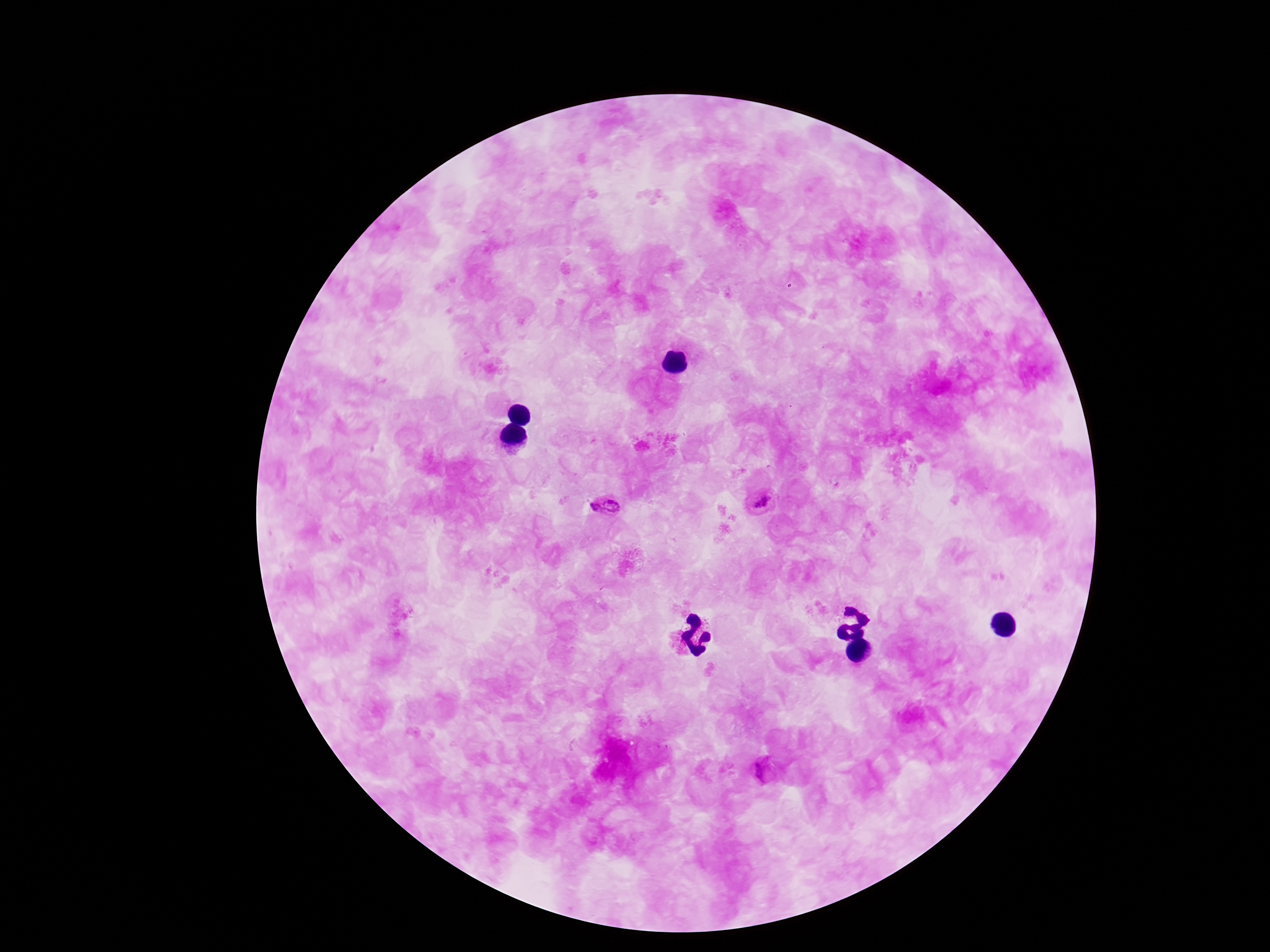
Approximate centers as [x, y] in pixels. Plasmodium parasite locations: [762, 505], [606, 509], [761, 771]. Smartphone photograph taken through the microscope eyepiece. Thick peripheral-blood smear. Giemsa stain. 100x magnification. Single field of view. Patient malaria status: positive. Image is 1270×952 pixels.